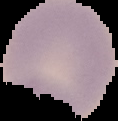
Result: no Plasmodium parasites detected. Image is 118×121 pixels. The area outside the segmented cell region is set to black. From a thin blood film.